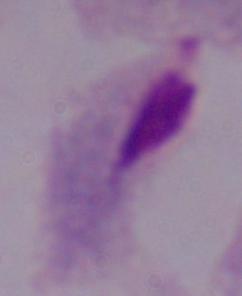

{
  "magnification": "1000x",
  "identification": "trichomonad",
  "modality": "micrograph"
}